State which parasite is depicted.
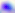

This is Toxoplasma gondii.

modality = photomicrograph
magnification = 400x